Give the position of every Plasmodium parasite visible.
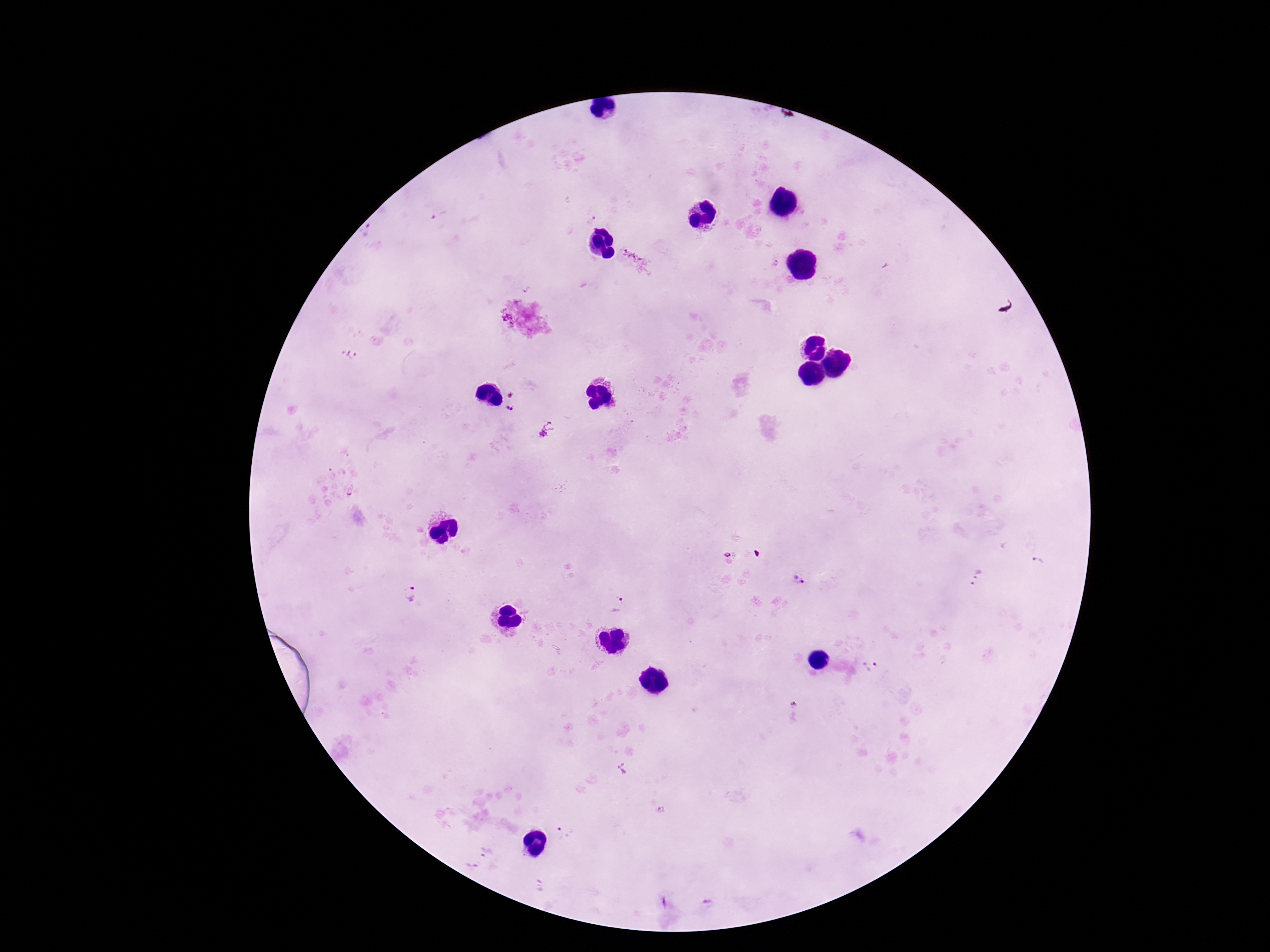

Approximate centers as {x, y} in pixels.
Plasmodium parasites: {438, 216}, {635, 259}, {774, 264}, {350, 354}, {511, 410}, {546, 430}, {729, 554}, {1043, 562}, {977, 577}, {798, 578}, {411, 592}, {617, 605}, {872, 667}, {794, 702}, {623, 769}, {662, 809}, {558, 830}, {485, 854}, {707, 903}.

capture = smartphone camera through the microscope eyepiece
stain = Giemsa
image size = 1270×952 pixels
preparation = thick blood smear
patient malaria status = infected
magnification = 100x
field of view = one from this slide